Identify the preparation type.
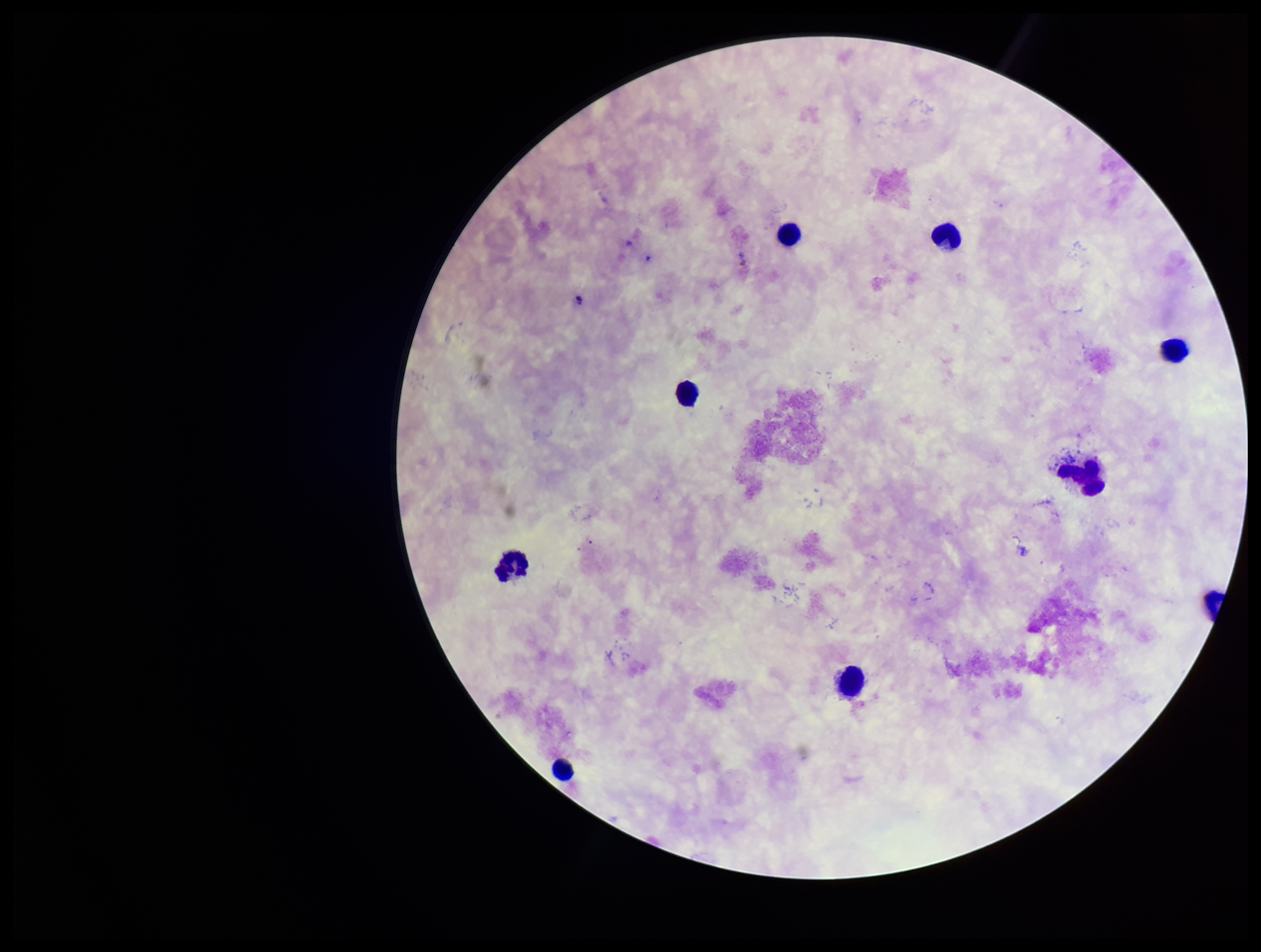
A thick smear.

Leukocyte count: 9. Smartphone photograph taken through the eyepiece of a microscope. Plasmodium parasites: none seen. Stained with Giemsa. One field from this slide. Image is 1261×952 pixels. Parasite count: 0. Patient malaria status: negative.